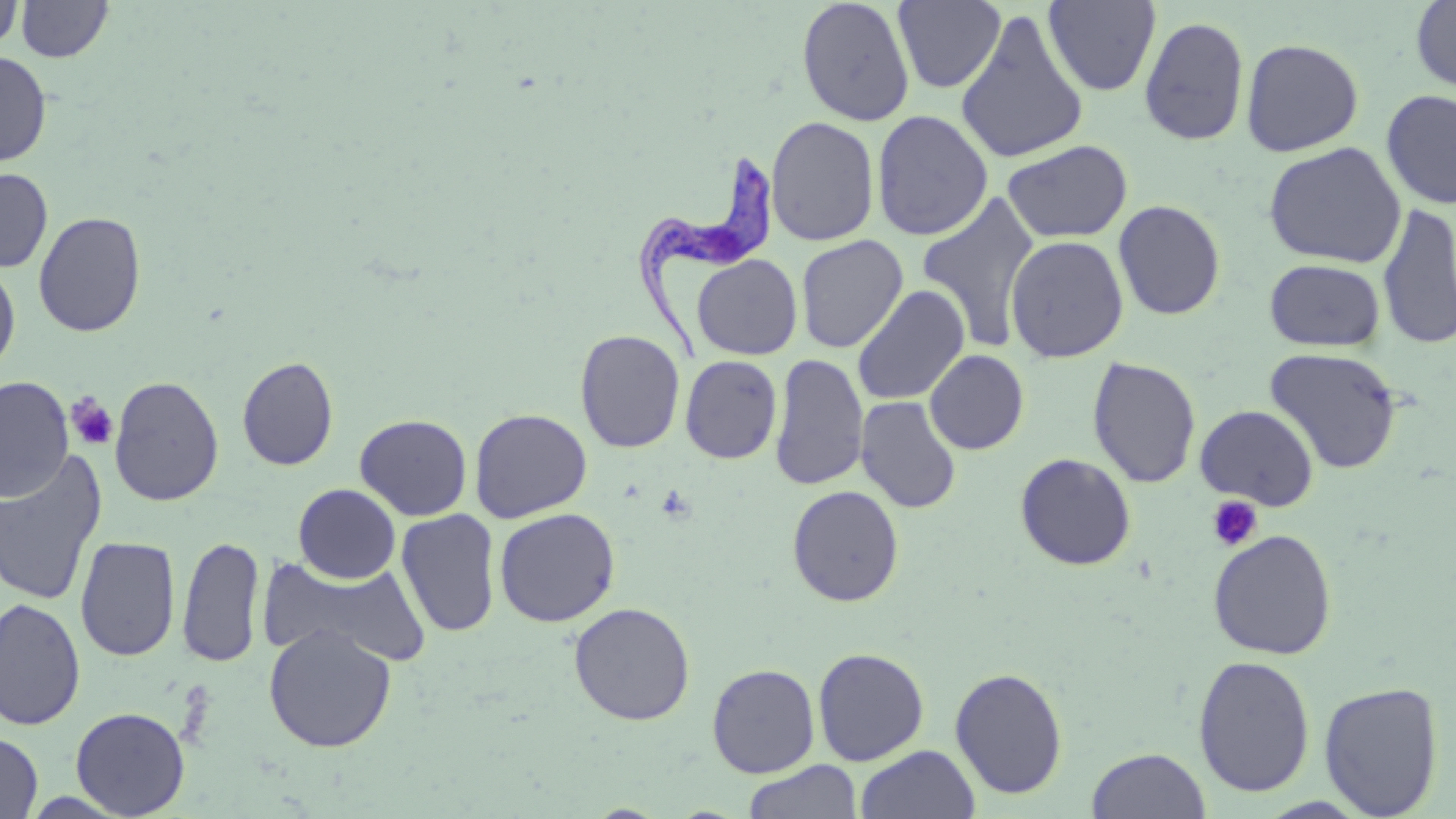
Approximate bounding boxes as named x1/y1/x2/y2 corners in pixels. Trypanosoma brucei locations: (x1=632, y1=150, x2=776, y2=361). Platelet locations: (x1=65, y1=393, x2=119, y2=451), (x1=1207, y1=495, x2=1263, y2=552). Uninfected red blood cell locations: (x1=796, y1=0, x2=915, y2=126), (x1=1411, y1=0, x2=1455, y2=94), (x1=0, y1=1, x2=23, y2=53), (x1=17, y1=1, x2=112, y2=62), (x1=892, y1=1, x2=1005, y2=93), (x1=1043, y1=1, x2=1161, y2=96), (x1=955, y1=9, x2=1089, y2=165), (x1=1138, y1=15, x2=1250, y2=147), (x1=1240, y1=38, x2=1364, y2=157), (x1=0, y1=50, x2=52, y2=166), (x1=1381, y1=88, x2=1456, y2=210), (x1=871, y1=109, x2=993, y2=241), (x1=766, y1=115, x2=880, y2=246), (x1=1002, y1=139, x2=1132, y2=242), (x1=1263, y1=141, x2=1406, y2=268), (x1=0, y1=168, x2=53, y2=272), (x1=916, y1=193, x2=1041, y2=351), (x1=1113, y1=200, x2=1226, y2=320), (x1=1376, y1=204, x2=1456, y2=351), (x1=33, y1=211, x2=146, y2=337), (x1=1005, y1=234, x2=1129, y2=363), (x1=795, y1=235, x2=909, y2=353), (x1=691, y1=254, x2=803, y2=360), (x1=1265, y1=258, x2=1386, y2=352), (x1=0, y1=260, x2=21, y2=376), (x1=851, y1=285, x2=970, y2=406), (x1=575, y1=329, x2=685, y2=453), (x1=1264, y1=347, x2=1404, y2=474), (x1=924, y1=350, x2=1029, y2=455), (x1=769, y1=353, x2=869, y2=490), (x1=680, y1=355, x2=782, y2=464), (x1=236, y1=356, x2=339, y2=471), (x1=1086, y1=356, x2=1202, y2=488), (x1=0, y1=376, x2=74, y2=503), (x1=109, y1=376, x2=225, y2=507), (x1=856, y1=395, x2=962, y2=514), (x1=1194, y1=404, x2=1319, y2=510), (x1=469, y1=407, x2=593, y2=523), (x1=354, y1=413, x2=473, y2=521), (x1=0, y1=451, x2=108, y2=607), (x1=1015, y1=452, x2=1137, y2=571), (x1=293, y1=483, x2=401, y2=584), (x1=787, y1=485, x2=905, y2=607), (x1=494, y1=507, x2=621, y2=627), (x1=396, y1=508, x2=501, y2=637), (x1=1208, y1=529, x2=1337, y2=660), (x1=75, y1=535, x2=180, y2=663), (x1=177, y1=536, x2=265, y2=668), (x1=258, y1=554, x2=432, y2=669), (x1=0, y1=598, x2=86, y2=731), (x1=568, y1=602, x2=696, y2=725), (x1=263, y1=624, x2=397, y2=752), (x1=812, y1=647, x2=929, y2=766), (x1=1192, y1=654, x2=1315, y2=797), (x1=706, y1=663, x2=820, y2=777), (x1=949, y1=666, x2=1068, y2=800), (x1=1318, y1=681, x2=1444, y2=818), (x1=71, y1=707, x2=190, y2=818), (x1=0, y1=731, x2=42, y2=819), (x1=855, y1=745, x2=980, y2=819), (x1=1087, y1=747, x2=1211, y2=819), (x1=743, y1=760, x2=862, y2=819). Slide-level diagnosis: Trypanosoma brucei. Thin blood film. 1000x magnification. May-Grünwald-Giemsa-stained preparation. Image is 1456×819 pixels. Light microscopy. One field of a larger specimen.